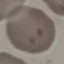

malaria status = parasitized
preparation = thin blood smear
image type = cell patch, automatically extracted from a larger field of view and resized to 64 × 64 pixels
stain = Giemsa
capture = smartphone through the microscope eyepiece